Locate every Trypanosoma brucei.
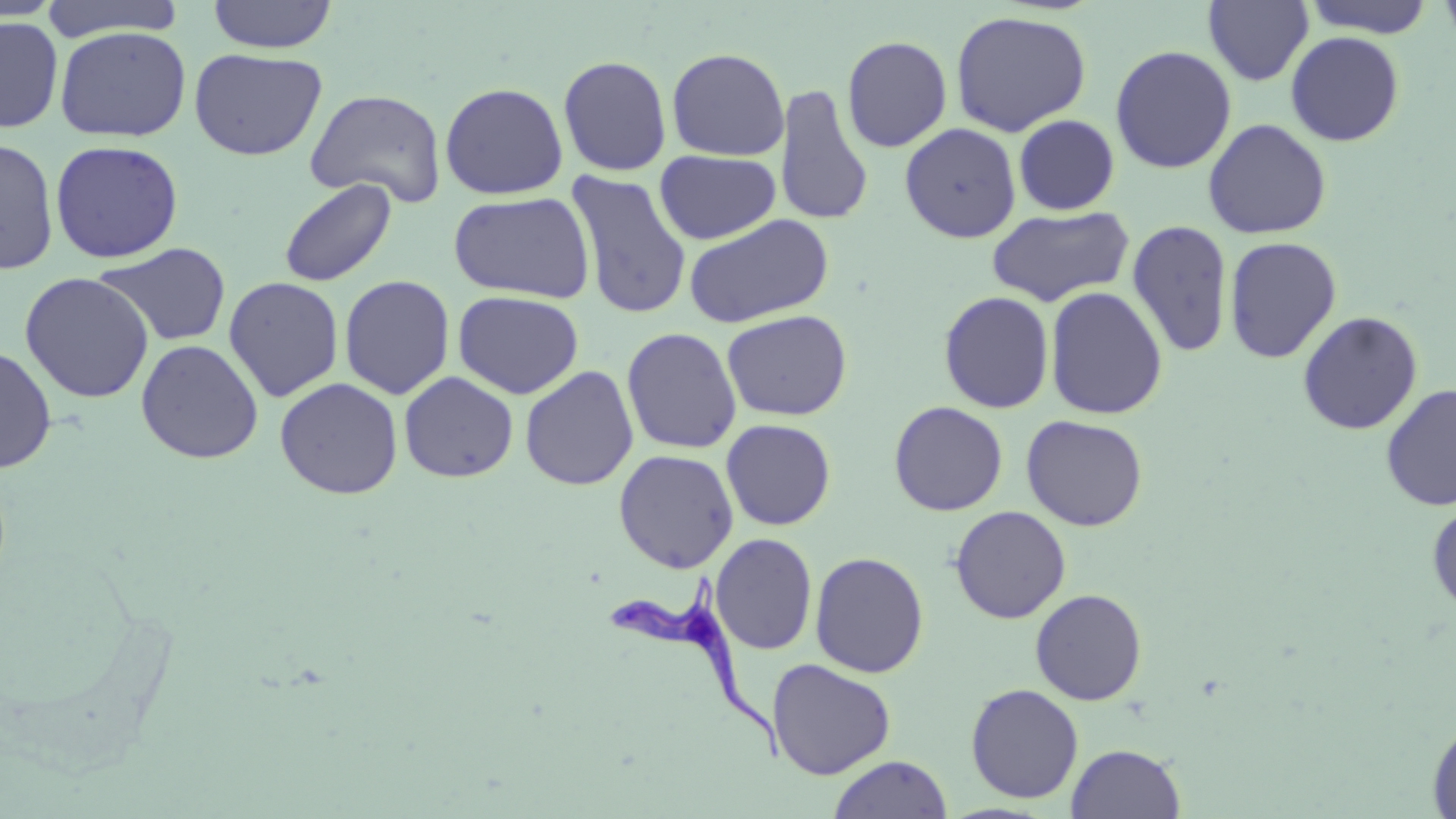
Approximate bounding boxes as [x1, y1, x2, y2] in pixels.
Trypanosoma brucei: [604, 579, 786, 766].

slide-level diagnosis = Trypanosoma brucei
field of view = single
modality = light microscopy
uninfected red blood cell locations = approximate bounding boxes as [x1, y1, x2, y2] in pixels: [38, 0, 189, 41], [1301, 0, 1437, 38], [1436, 0, 1456, 49], [207, 1, 337, 53], [1203, 1, 1313, 86], [950, 10, 1092, 136], [0, 16, 63, 133], [54, 26, 191, 141], [1285, 30, 1405, 146], [841, 36, 952, 153], [1109, 45, 1237, 174], [666, 47, 790, 161], [189, 48, 327, 160], [557, 55, 673, 176], [440, 82, 569, 199], [774, 84, 874, 227], [306, 88, 447, 209], [1013, 114, 1120, 215], [1203, 118, 1332, 239], [900, 122, 1021, 243], [0, 138, 59, 275], [49, 139, 184, 263], [654, 150, 781, 244], [566, 171, 692, 320], [279, 178, 397, 287], [448, 191, 596, 303], [986, 206, 1134, 307], [683, 213, 834, 328], [1127, 219, 1234, 358], [1223, 236, 1342, 364], [93, 243, 232, 347], [19, 272, 155, 403], [339, 275, 455, 400], [224, 276, 344, 402], [1045, 286, 1168, 420], [453, 290, 584, 399], [938, 291, 1055, 414], [722, 309, 852, 421], [1297, 311, 1423, 435], [621, 327, 742, 454], [136, 339, 264, 463], [0, 346, 57, 473], [520, 365, 639, 491], [399, 371, 518, 483], [275, 377, 403, 499], [1380, 383, 1456, 511], [889, 401, 1008, 516], [1021, 414, 1148, 531], [721, 419, 836, 530], [613, 449, 739, 573], [1427, 501, 1456, 616], [950, 506, 1071, 623], [710, 533, 817, 655], [810, 551, 929, 678], [1030, 588, 1147, 705], [766, 658, 896, 780], [965, 683, 1084, 803], [1426, 716, 1456, 818], [1066, 743, 1186, 818], [827, 754, 953, 819]
preparation = thin blood film
stain = May-Grünwald-Giemsa
magnification = 1000x
image size = 1456×819 pixels